Classify this cell by malaria status.
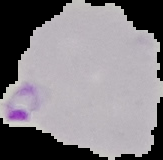

It is parasitized.

image type = segmented cell region on a black background
preparation = thin blood smear
image size = 163×160 pixels